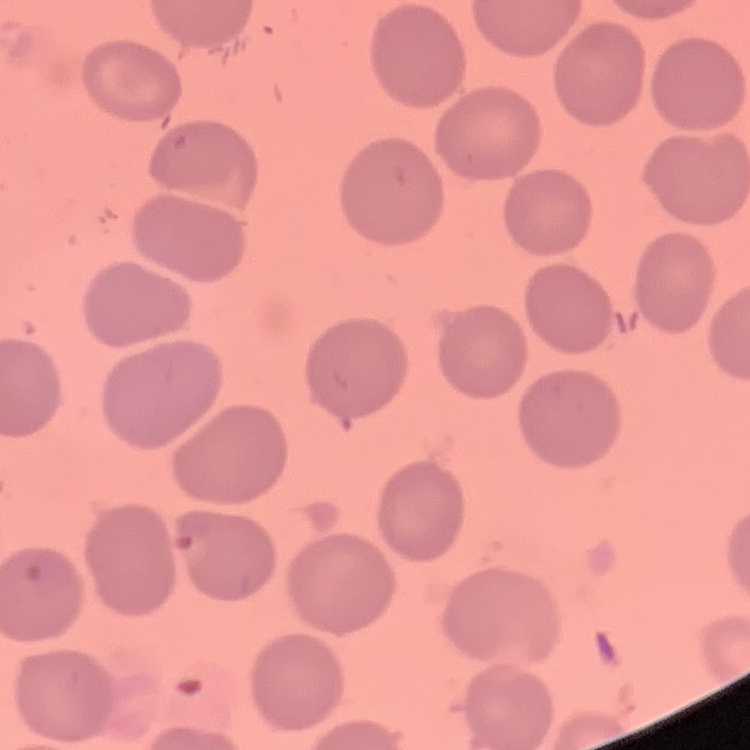 The red blood cells show no rouleaux formation. One tile cut from a larger photomicrograph. Thin blood smear. Field's or Giemsa stain.